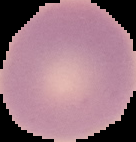

Image is 136×142 pixels. From a thin blood film. Malaria status: uninfected. The area outside the segmented cell region is set to black.